Mark where leukocytes are.
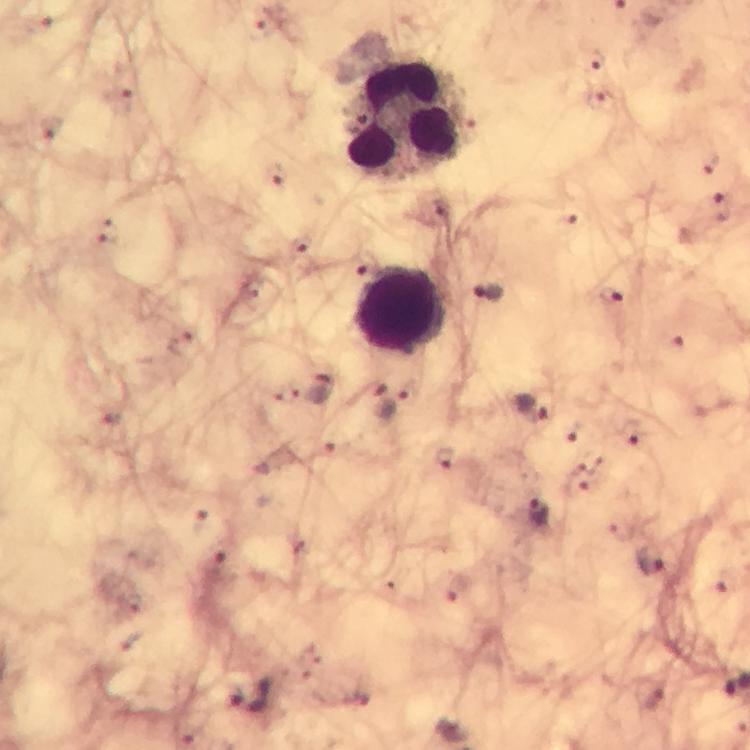

Approximate centers as [x, y] in pixels.
Leukocytes: [403, 117], [401, 309].

Plasmodium parasite locations: [596, 60], [603, 101], [720, 209], [488, 291], [321, 389], [383, 403], [531, 407], [445, 456], [538, 512], [651, 563], [251, 697]. Photographed with a smartphone mounted on the microscope. 100x magnification. From a diagnostic examination for malaria. A crop from one field of view. Immersion oil applied. Image is 750×750 pixels. Thick blood smear. Giemsa-stained preparation.